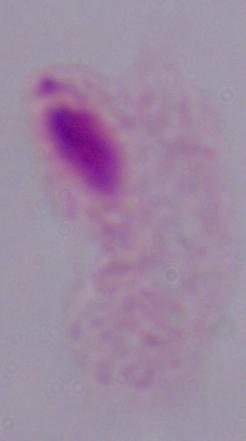

magnification = 1000x
identification = trichomonad
modality = photomicrograph